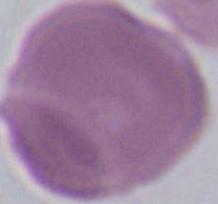
Micrograph. 1000x magnification. A red blood cell is shown.